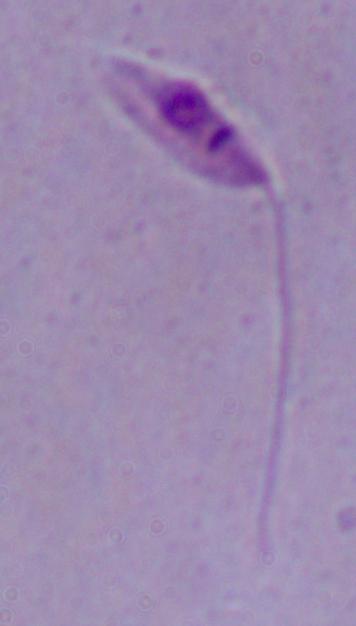 A Leishmania parasite is shown. Micrograph. Captured at 1000x magnification.